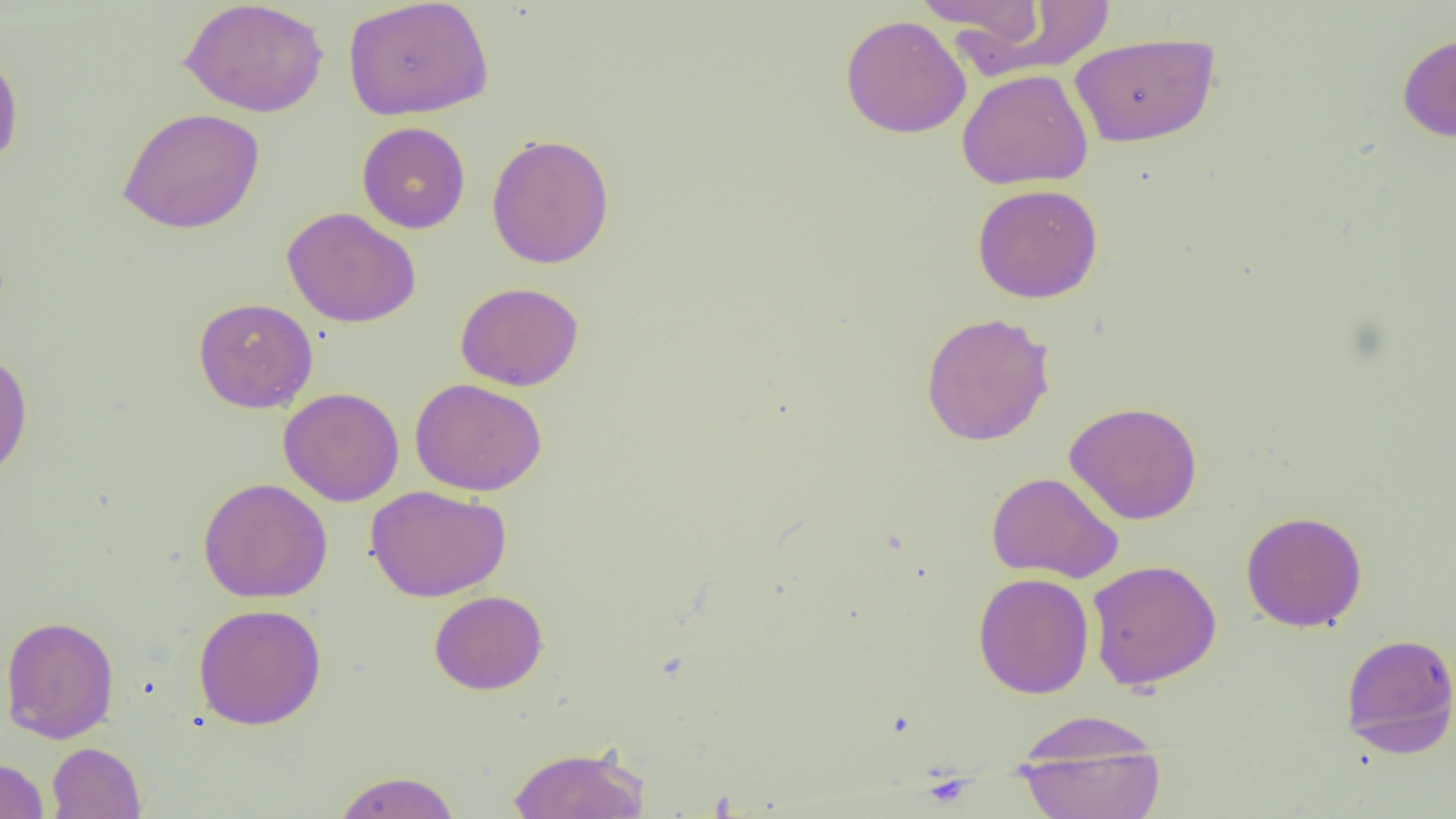

{
  "slide_level_diagnosis": "negative for blood parasites",
  "uninfected_red_blood_cell_locations": "approximate bounding boxes as [x1, y1, x2, y2] in pixels: [179, 0, 329, 118], [342, 0, 494, 121], [912, 1, 1045, 39], [964, 1, 1117, 77], [840, 14, 971, 139], [1069, 32, 1220, 147], [1396, 32, 1456, 143], [0, 50, 24, 171], [956, 68, 1094, 190], [116, 107, 265, 234], [357, 121, 471, 234], [486, 133, 615, 269], [971, 183, 1104, 304], [282, 206, 421, 328], [455, 282, 584, 391], [192, 297, 318, 413], [919, 312, 1055, 446], [0, 350, 34, 485], [409, 377, 547, 496], [278, 387, 405, 507], [1064, 401, 1203, 525], [985, 471, 1123, 584], [197, 477, 333, 603], [365, 485, 511, 602], [1240, 511, 1368, 633], [1086, 559, 1222, 690], [973, 572, 1094, 699], [429, 590, 548, 695], [193, 603, 327, 730], [1, 614, 120, 744], [1340, 631, 1456, 758], [1011, 710, 1163, 777], [1014, 734, 1165, 819], [47, 742, 146, 819], [506, 744, 650, 818], [0, 757, 48, 819], [332, 770, 462, 818]",
  "preparation": "thin blood smear",
  "modality": "optical microscopy",
  "image_size": "1456×819 pixels",
  "field_of_view": "single",
  "magnification": "1000x"
}